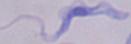
Summary:
  - Modality: micrograph
  - Identification: trypanosome
  - Magnification: 1000x